Locate and identify every blood parasite.
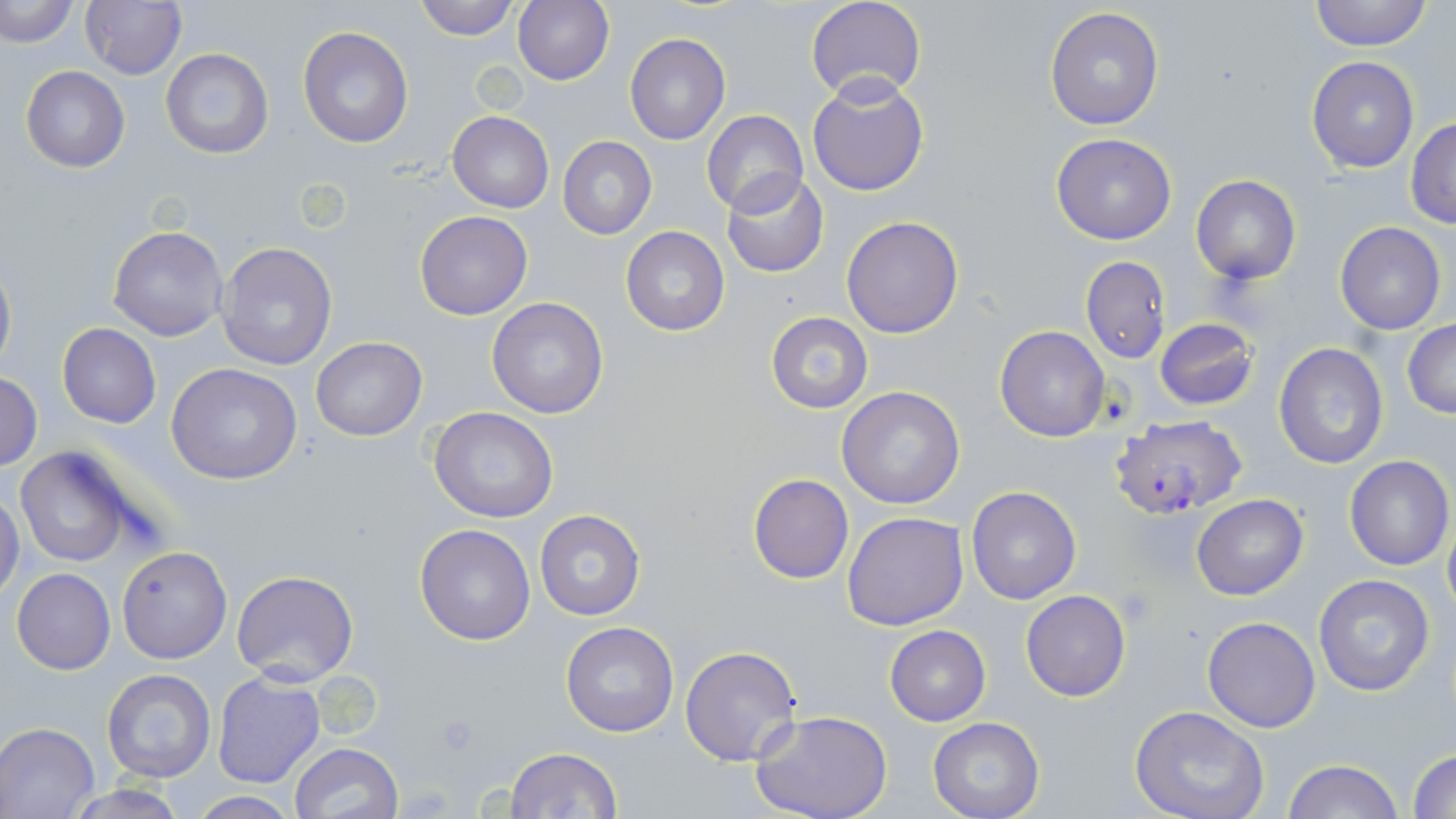

Approximate bounding boxes as (x1, y1, x2, y2) in pixels.
Plasmodium falciparum-infected red blood cells: (1111, 415, 1246, 518).
No Plasmodium ovale, Plasmodium malariae, Plasmodium vivax, Babesia divergens, or Trypanosoma brucei observed.

Uninfected red blood cell locations: (1, 0, 76, 46), (79, 0, 186, 81), (412, 0, 518, 39), (805, 0, 927, 103), (1308, 0, 1432, 51), (512, 1, 614, 85), (1044, 8, 1165, 129), (298, 27, 415, 149), (624, 32, 731, 145), (160, 48, 274, 159), (1306, 57, 1419, 172), (20, 67, 129, 174), (808, 78, 929, 197), (701, 109, 808, 215), (447, 111, 554, 212), (1406, 118, 1456, 228), (1050, 134, 1177, 245), (558, 136, 657, 238), (722, 172, 829, 278), (1190, 175, 1302, 285), (415, 211, 533, 319), (842, 216, 964, 338), (1334, 223, 1446, 334), (621, 225, 729, 337), (108, 226, 228, 341), (216, 241, 339, 372), (1079, 255, 1169, 364), (0, 257, 15, 378), (487, 297, 608, 420), (766, 311, 873, 414), (1154, 318, 1259, 412), (1402, 321, 1456, 419), (57, 324, 161, 429), (994, 325, 1110, 442), (310, 337, 428, 440), (1273, 343, 1389, 468), (167, 363, 302, 485), (0, 373, 43, 469), (838, 386, 966, 510), (429, 405, 560, 522), (14, 444, 141, 568), (1344, 456, 1454, 571), (747, 474, 854, 584), (966, 486, 1082, 604), (0, 488, 24, 603), (1192, 494, 1308, 600), (533, 508, 645, 621), (843, 511, 968, 629), (1443, 515, 1456, 618), (414, 523, 536, 645), (117, 546, 231, 664), (11, 568, 116, 675), (232, 570, 359, 685), (1313, 573, 1438, 697), (1021, 589, 1131, 702), (1202, 616, 1320, 733), (561, 620, 678, 737), (884, 625, 991, 727), (680, 645, 803, 766), (100, 669, 216, 783), (210, 672, 325, 789), (1130, 706, 1274, 819), (752, 712, 893, 819), (928, 717, 1045, 819), (0, 723, 100, 817), (289, 742, 403, 819), (504, 747, 620, 819), (1408, 747, 1456, 818), (1283, 759, 1403, 819), (60, 784, 192, 818), (186, 793, 301, 818). Platelet locations: (434, 712, 483, 758). Slide-level diagnosis: Plasmodium falciparum. May-Grünwald-Giemsa-stained preparation. Image is 1456×819 pixels. Single field of view. Optical microscopy. Thin blood smear. Captured at 1000x magnification.